Outline each blood parasite and name the species.
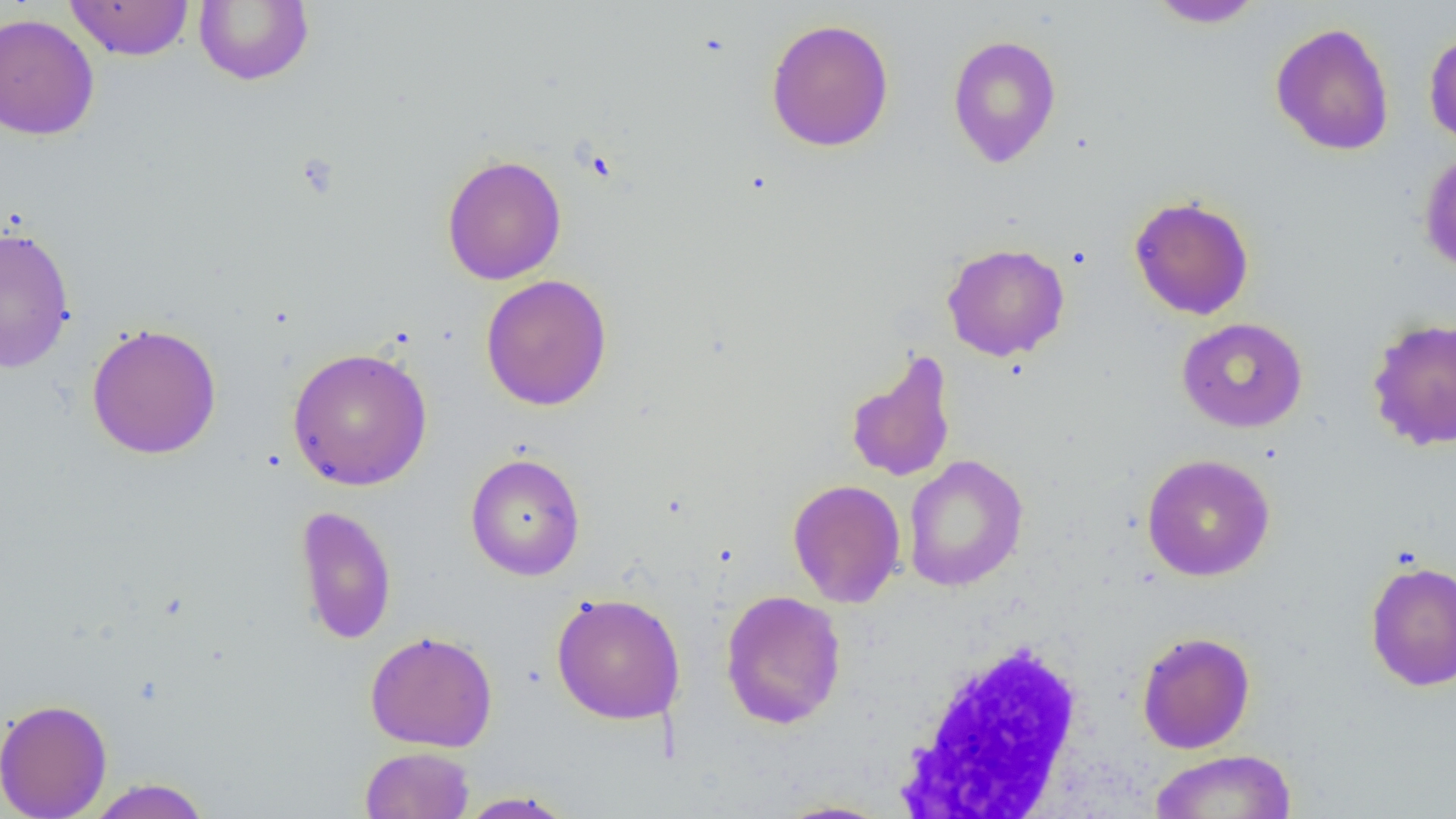

No blood parasites observed.

Approximate bounding boxes as named x1/y1/x2/y2 corners in pixels. Uninfected red blood cell locations: (x1=64, y1=0, x2=194, y2=61), (x1=193, y1=0, x2=314, y2=86), (x1=1146, y1=0, x2=1265, y2=29), (x1=0, y1=13, x2=100, y2=140), (x1=765, y1=18, x2=895, y2=152), (x1=1270, y1=22, x2=1395, y2=156), (x1=1423, y1=29, x2=1456, y2=149), (x1=947, y1=34, x2=1062, y2=168), (x1=1419, y1=149, x2=1456, y2=275), (x1=441, y1=154, x2=567, y2=285), (x1=1129, y1=195, x2=1254, y2=320), (x1=0, y1=225, x2=75, y2=373), (x1=941, y1=242, x2=1070, y2=361), (x1=480, y1=274, x2=613, y2=411), (x1=1366, y1=316, x2=1456, y2=452), (x1=1176, y1=317, x2=1308, y2=432), (x1=86, y1=322, x2=222, y2=460), (x1=288, y1=347, x2=432, y2=491), (x1=844, y1=349, x2=958, y2=484), (x1=465, y1=453, x2=586, y2=581), (x1=1141, y1=453, x2=1276, y2=582), (x1=902, y1=454, x2=1028, y2=592), (x1=787, y1=478, x2=906, y2=608), (x1=294, y1=504, x2=397, y2=645), (x1=1365, y1=559, x2=1456, y2=692), (x1=720, y1=589, x2=847, y2=730), (x1=550, y1=592, x2=686, y2=725), (x1=365, y1=630, x2=498, y2=752), (x1=1137, y1=631, x2=1255, y2=754), (x1=0, y1=698, x2=113, y2=819), (x1=360, y1=746, x2=475, y2=818), (x1=1148, y1=750, x2=1297, y2=818), (x1=84, y1=777, x2=212, y2=819), (x1=454, y1=790, x2=578, y2=818), (x1=773, y1=799, x2=892, y2=818). White blood cell locations: (x1=896, y1=636, x2=1090, y2=817). Slide-level diagnosis: negative for blood parasites. 1000x magnification. Optical microscopy. Single field of view. Image is 1456×819 pixels. Thin blood film.